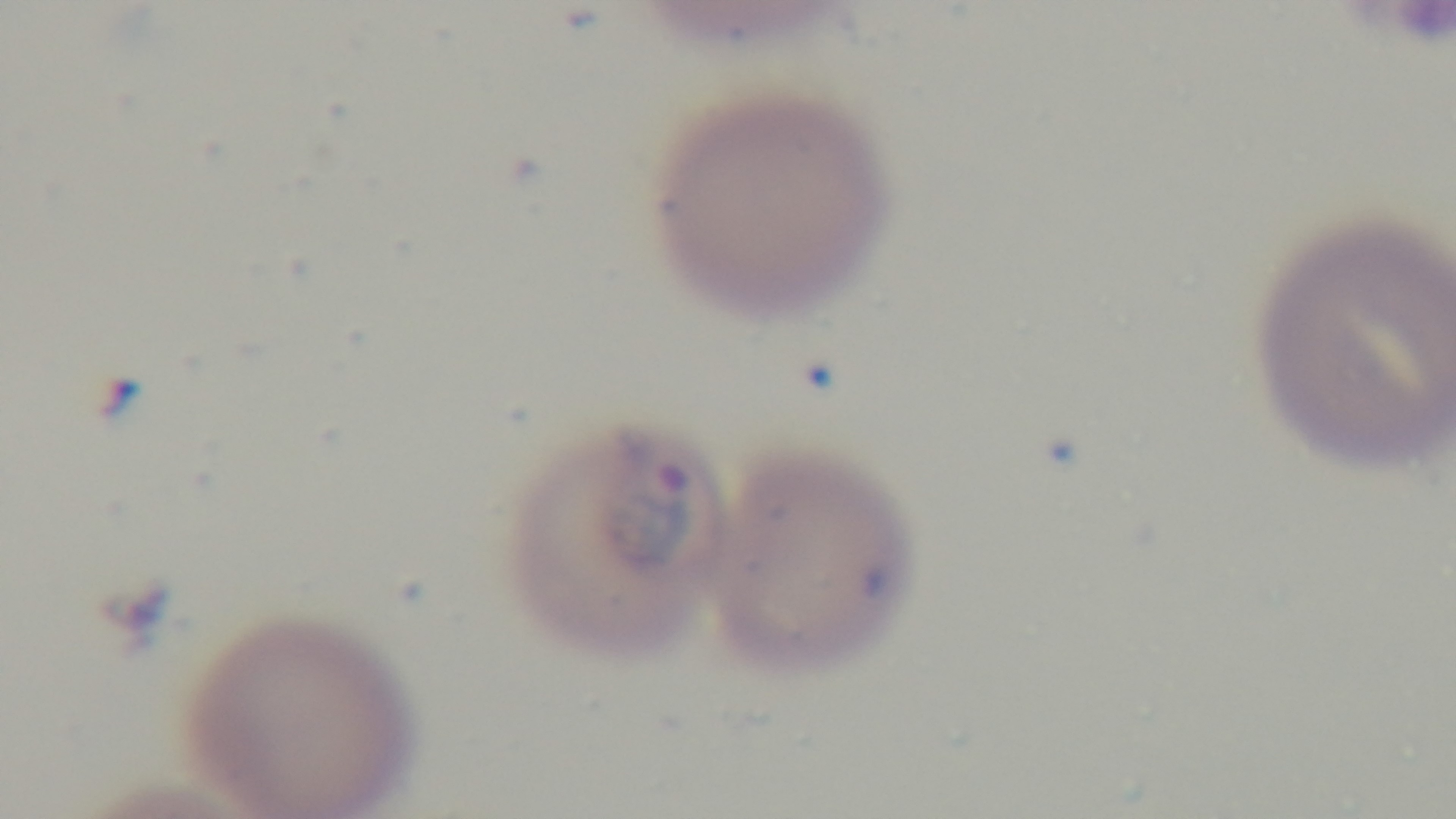
Giemsa stain. Single field of view. Light microscopy. Preparation: thin blood film. Malaria status: infected. Mounted 4K digital camera. Oil-immersion objective, 100x.